Locate and identify every blood parasite.
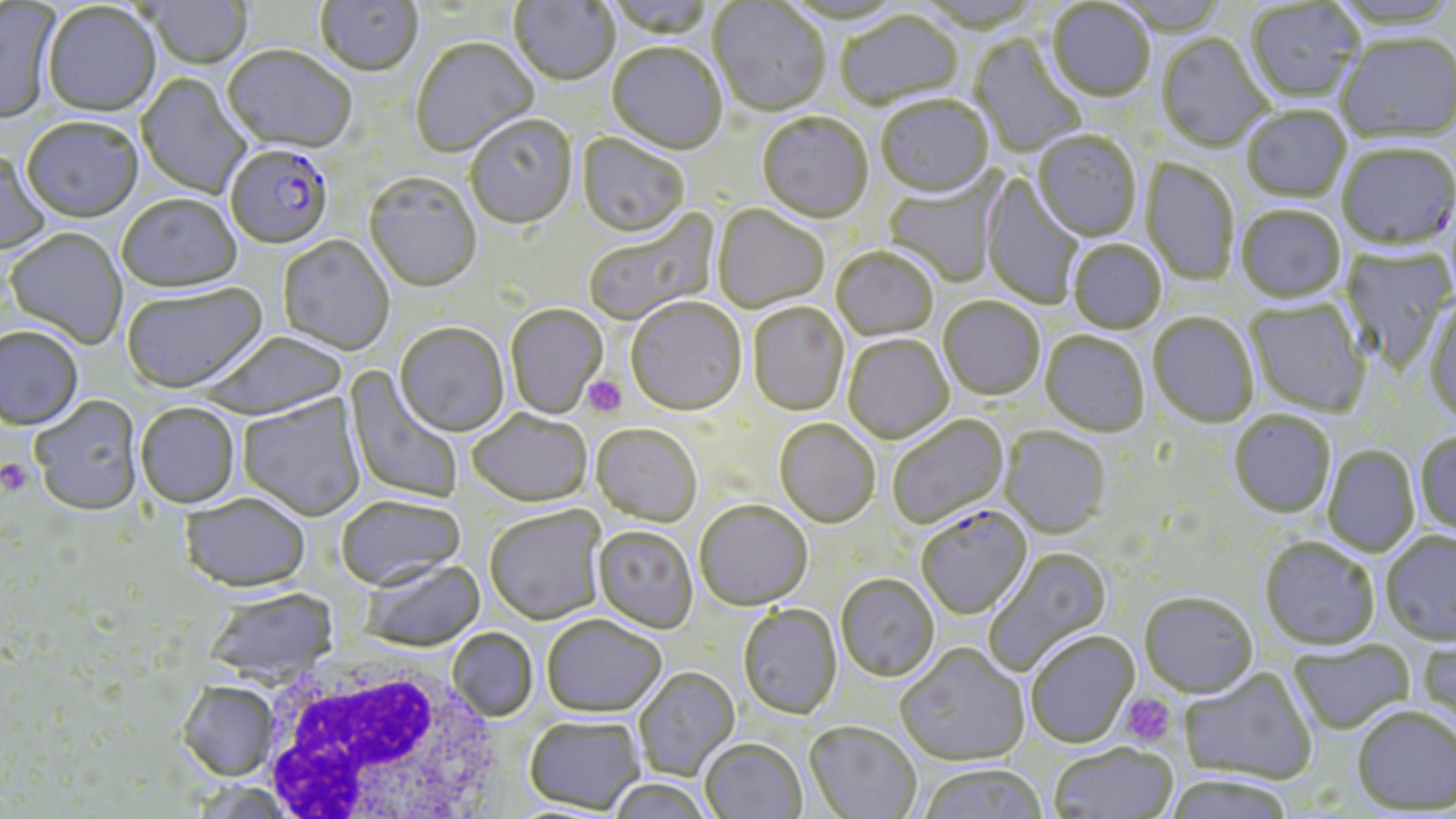
Approximate bounding boxes as named x1/y1/x2/y2 corners in pixels.
Plasmodium falciparum-infected red blood cells: (x1=1337, y1=142, x2=1456, y2=251), (x1=226, y1=148, x2=333, y2=251), (x1=916, y1=506, x2=1034, y2=621).
No Plasmodium ovale, Plasmodium malariae, Plasmodium vivax, Babesia divergens, or Trypanosoma brucei observed.

Summary:
  - Platelet locations: (x1=581, y1=374, x2=628, y2=418), (x1=0, y1=459, x2=34, y2=496), (x1=1119, y1=693, x2=1177, y2=748)
  - White blood cell locations: (x1=254, y1=655, x2=509, y2=819)
  - Uninfected red blood cell locations: (x1=314, y1=0, x2=424, y2=79), (x1=509, y1=0, x2=618, y2=88), (x1=605, y1=0, x2=717, y2=41), (x1=1113, y1=0, x2=1229, y2=35), (x1=1330, y1=0, x2=1456, y2=30), (x1=141, y1=1, x2=254, y2=71), (x1=780, y1=1, x2=908, y2=26), (x1=1245, y1=1, x2=1366, y2=102), (x1=708, y1=2, x2=830, y2=118), (x1=1046, y1=2, x2=1156, y2=102), (x1=0, y1=3, x2=59, y2=125), (x1=42, y1=4, x2=161, y2=119), (x1=835, y1=12, x2=964, y2=110), (x1=1336, y1=32, x2=1455, y2=143), (x1=1157, y1=34, x2=1272, y2=153), (x1=970, y1=35, x2=1087, y2=158), (x1=411, y1=39, x2=539, y2=159), (x1=606, y1=45, x2=727, y2=156), (x1=221, y1=48, x2=356, y2=156), (x1=136, y1=74, x2=251, y2=199), (x1=876, y1=97, x2=994, y2=200), (x1=1241, y1=106, x2=1352, y2=202), (x1=757, y1=114, x2=874, y2=225), (x1=465, y1=118, x2=578, y2=231), (x1=21, y1=121, x2=143, y2=224), (x1=1032, y1=130, x2=1142, y2=242), (x1=577, y1=134, x2=689, y2=239), (x1=0, y1=150, x2=51, y2=256), (x1=1141, y1=158, x2=1240, y2=287), (x1=981, y1=172, x2=1085, y2=310), (x1=883, y1=173, x2=1005, y2=288), (x1=363, y1=174, x2=482, y2=294), (x1=117, y1=196, x2=242, y2=294), (x1=1236, y1=205, x2=1346, y2=303), (x1=712, y1=206, x2=829, y2=314), (x1=582, y1=210, x2=719, y2=328), (x1=4, y1=229, x2=128, y2=350), (x1=277, y1=237, x2=394, y2=356), (x1=1068, y1=239, x2=1167, y2=333), (x1=1340, y1=246, x2=1456, y2=375), (x1=831, y1=248, x2=939, y2=342), (x1=122, y1=284, x2=268, y2=396), (x1=938, y1=297, x2=1045, y2=400), (x1=1424, y1=298, x2=1456, y2=427), (x1=626, y1=299, x2=747, y2=418), (x1=1245, y1=299, x2=1372, y2=417), (x1=748, y1=303, x2=849, y2=417), (x1=505, y1=305, x2=608, y2=420), (x1=1148, y1=311, x2=1259, y2=427), (x1=395, y1=325, x2=509, y2=438), (x1=1, y1=327, x2=84, y2=432), (x1=1041, y1=331, x2=1150, y2=437), (x1=202, y1=333, x2=349, y2=422), (x1=843, y1=335, x2=954, y2=445), (x1=343, y1=365, x2=465, y2=506), (x1=238, y1=394, x2=365, y2=522), (x1=29, y1=397, x2=144, y2=517), (x1=135, y1=404, x2=240, y2=509), (x1=1229, y1=410, x2=1336, y2=517), (x1=467, y1=411, x2=592, y2=509), (x1=887, y1=415, x2=1009, y2=530), (x1=774, y1=420, x2=880, y2=529), (x1=591, y1=426, x2=702, y2=527), (x1=1000, y1=426, x2=1111, y2=540), (x1=1414, y1=430, x2=1456, y2=536), (x1=1322, y1=445, x2=1420, y2=557), (x1=180, y1=496, x2=311, y2=595), (x1=336, y1=496, x2=466, y2=593), (x1=695, y1=503, x2=812, y2=611), (x1=485, y1=508, x2=606, y2=626), (x1=593, y1=527, x2=698, y2=634), (x1=1380, y1=531, x2=1456, y2=644), (x1=1260, y1=538, x2=1380, y2=650), (x1=983, y1=547, x2=1113, y2=677), (x1=358, y1=561, x2=486, y2=653), (x1=836, y1=575, x2=939, y2=682), (x1=204, y1=589, x2=339, y2=687), (x1=1139, y1=592, x2=1259, y2=698), (x1=737, y1=605, x2=842, y2=720), (x1=542, y1=618, x2=667, y2=719), (x1=447, y1=628, x2=538, y2=722), (x1=1025, y1=631, x2=1139, y2=748), (x1=1417, y1=635, x2=1456, y2=740), (x1=1288, y1=640, x2=1414, y2=735), (x1=897, y1=644, x2=1029, y2=766), (x1=1179, y1=667, x2=1317, y2=785), (x1=634, y1=669, x2=740, y2=780), (x1=176, y1=682, x2=279, y2=782), (x1=1351, y1=705, x2=1455, y2=814), (x1=524, y1=718, x2=644, y2=814), (x1=804, y1=723, x2=921, y2=819), (x1=700, y1=740, x2=806, y2=819), (x1=1048, y1=744, x2=1177, y2=819), (x1=918, y1=763, x2=1047, y2=819), (x1=1164, y1=774, x2=1296, y2=819), (x1=606, y1=780, x2=716, y2=819)
  - Slide-level diagnosis: Plasmodium falciparum
  - Image size: 1456×819 pixels
  - Modality: optical microscopy
  - Magnification: 1000x
  - Stain: May-Grünwald-Giemsa
  - Preparation: thin blood film
  - Field of view: one of a larger specimen